State the preparation type.
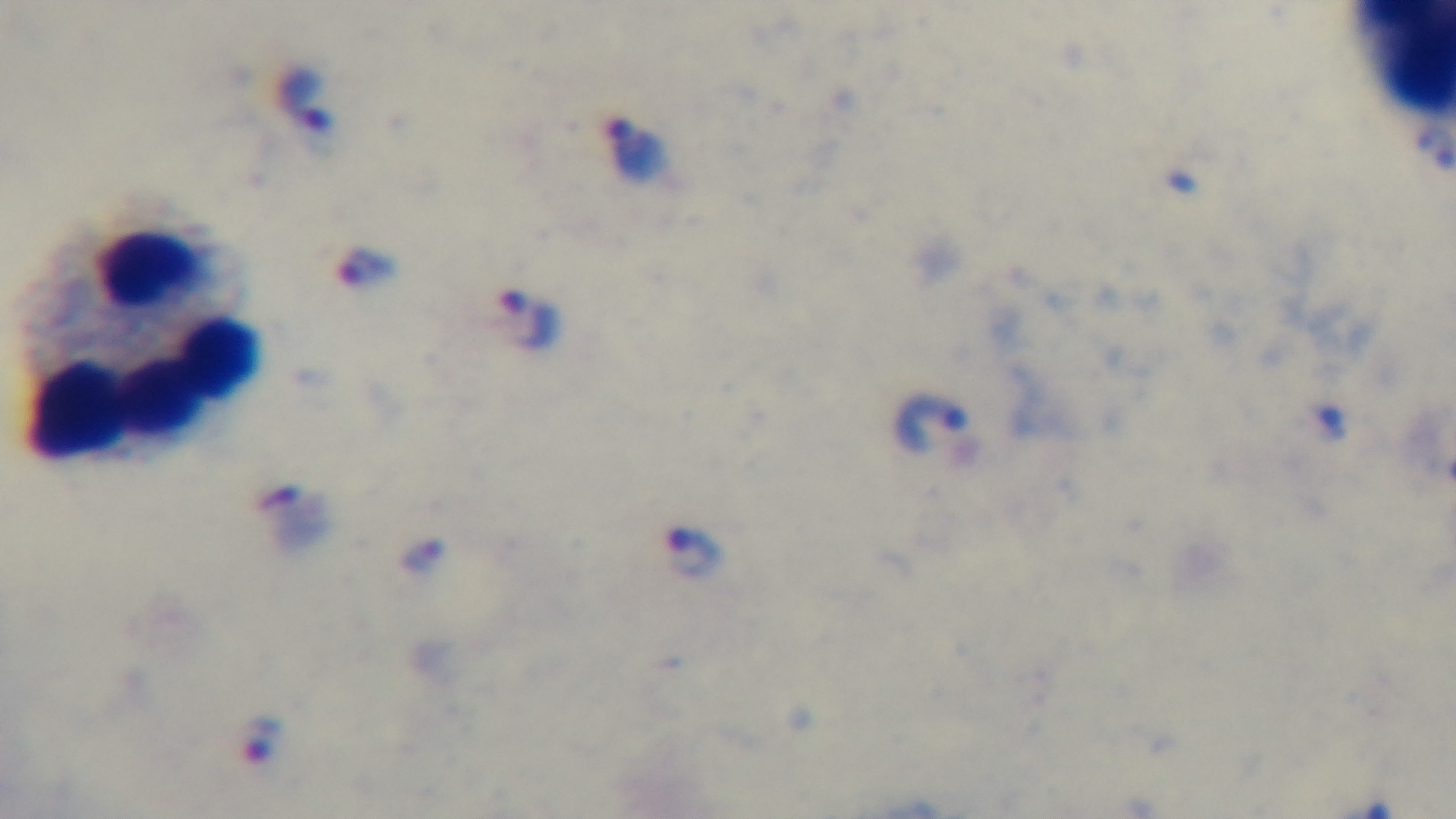
Thick.

modality: light microscopy
capture: mounted 4K digital camera
objective: 100x oil immersion
field_of_view: single
malaria_status: infected
stain: Giemsa